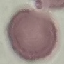
malaria status = uninfected
preparation = thin blood film
image type = automatically extracted cell patch, resized to 64 × 64 pixels
capture = smartphone camera at the microscope eyepiece
stain = Giemsa